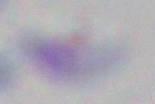

modality: photomicrograph
magnification: 1000x
identification: Toxoplasma gondii